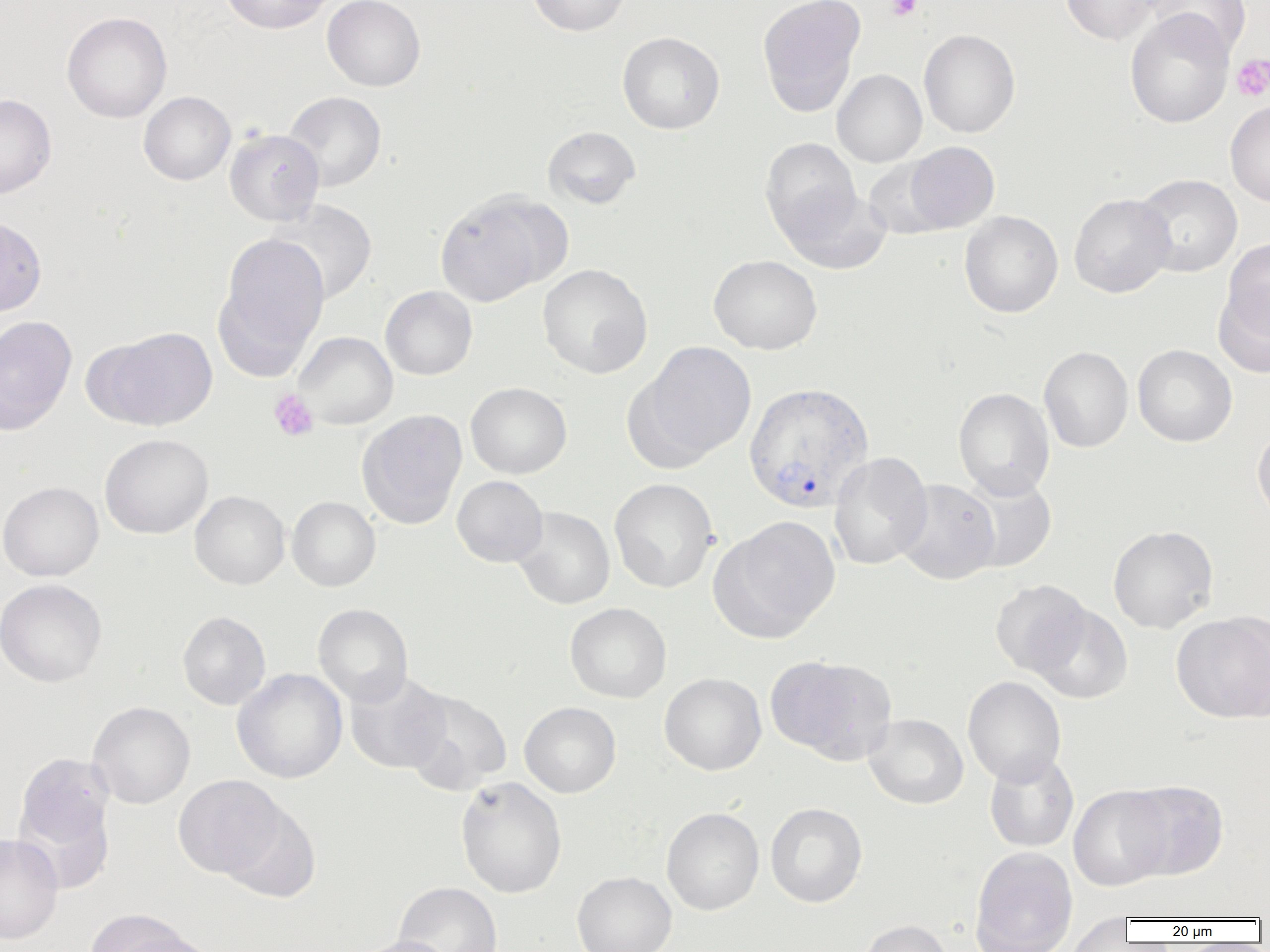
slide-level diagnosis = Plasmodium vivax
modality = optical microscopy
preparation = thin blood smear
uninfected red blood cell locations = approximate bounding boxes as (x1,y1)-(x2,y2) corner pairs in pixels: (218,0)-(334,34), (322,0)-(426,91), (525,0)-(632,36), (757,0)-(866,117), (1060,0)-(1165,45), (1144,0)-(1252,58), (1125,9)-(1235,128), (62,11)-(172,123), (919,29)-(1020,138), (617,31)-(725,134), (831,69)-(927,167), (138,91)-(236,185), (283,91)-(386,192), (0,93)-(57,199), (1225,100)-(1270,207), (542,126)-(641,209), (224,129)-(324,226), (759,137)-(861,241), (904,141)-(1000,232), (863,158)-(953,240), (1133,173)-(1243,277), (779,186)-(892,274), (434,193)-(557,307), (1069,193)-(1176,298), (269,200)-(378,304), (959,211)-(1063,317), (0,215)-(46,317), (216,232)-(330,368), (1220,238)-(1270,344), (708,254)-(822,355), (537,264)-(653,379), (1213,283)-(1270,379), (380,285)-(478,380), (0,315)-(77,434), (96,326)-(218,431), (293,331)-(398,429), (635,340)-(757,464), (1132,344)-(1237,447), (1038,345)-(1134,453), (465,382)-(572,479), (953,387)-(1055,499), (357,409)-(468,529), (1252,424)-(1270,528), (99,433)-(214,539), (828,451)-(933,570), (958,473)-(1057,573), (452,475)-(548,567), (609,478)-(719,593), (894,479)-(1000,584), (0,481)-(104,581), (189,490)-(290,589), (286,496)-(380,591), (512,506)-(615,609), (713,515)-(841,642), (1108,525)-(1218,633), (0,579)-(107,688), (990,580)-(1092,677), (312,603)-(413,706), (565,603)-(672,703), (1029,603)-(1133,704), (177,611)-(271,710), (1171,611)-(1270,723), (766,654)-(898,766), (231,668)-(348,783), (343,671)-(452,774), (659,672)-(766,775), (962,676)-(1066,786), (401,688)-(512,795), (87,701)-(195,809), (519,701)-(621,797), (863,713)-(969,809), (984,751)-(1079,852), (14,752)-(116,865), (173,775)-(286,879), (455,776)-(567,898), (1121,780)-(1229,880), (1068,785)-(1172,891), (219,801)-(322,903), (765,802)-(867,908), (661,806)-(764,915), (0,833)-(63,943), (970,847)-(1078,950), (572,871)-(676,952), (393,881)-(503,952), (85,910)-(197,952), (1064,914)-(1135,951), (856,919)-(955,952), (112,930)-(222,952), (349,935)-(457,952)
magnification = 1000x
Plasmodium vivax-infected red blood cell locations = approximate bounding boxes as (x1,y1)-(x2,y2) corner pairs in pixels: (743,382)-(874,513)
platelet locations = approximate bounding boxes as (x1,y1)-(x2,y2) corner pairs in pixels: (886,0)-(922,21), (1231,54)-(1270,101), (269,389)-(319,441)
image size = 1270×952 pixels
field of view = single